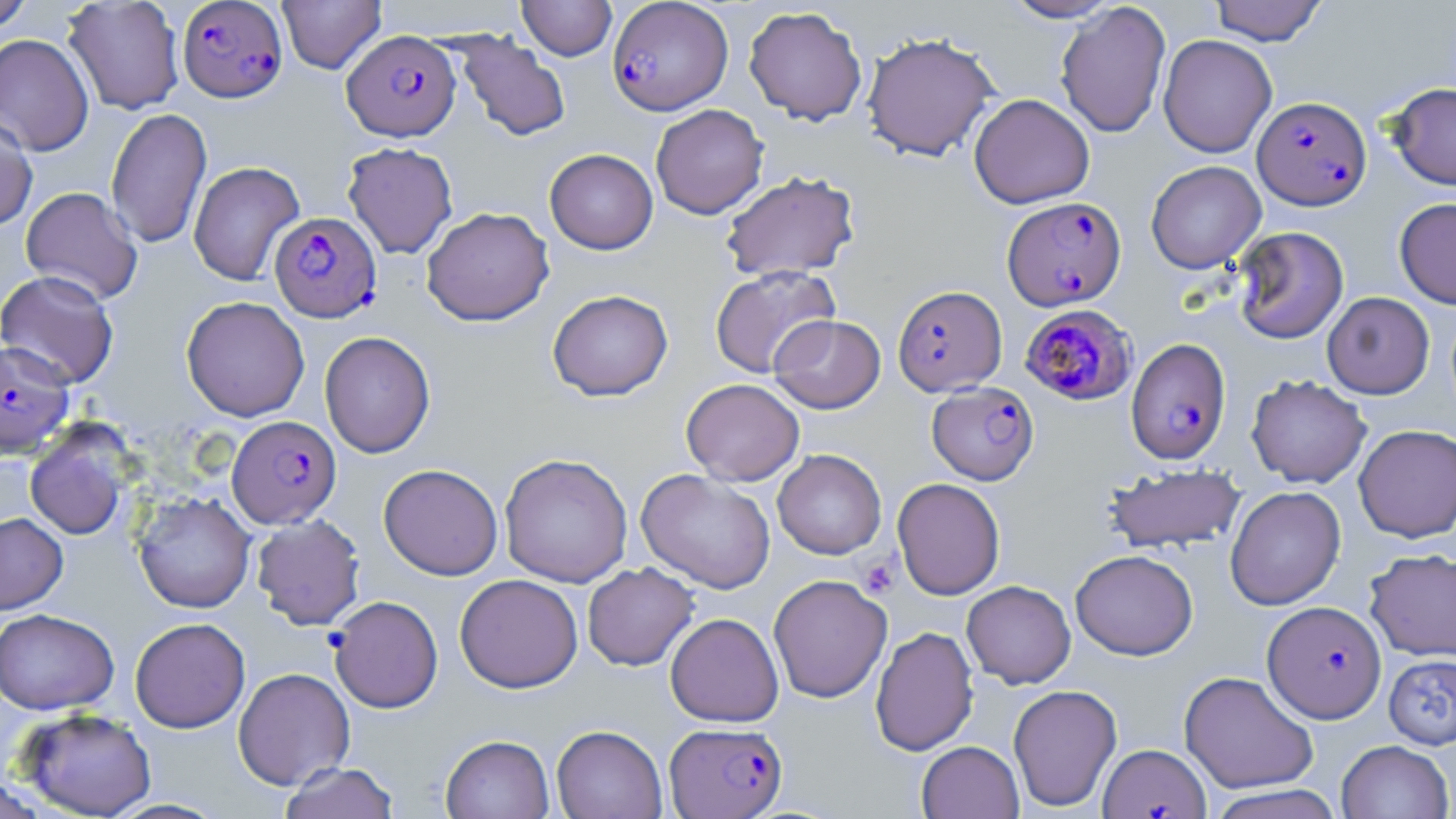 Approximate bounding boxes as (x1,y1)-(x2,y2) corner pairs in pixels. Uninfected red blood cell locations: (62,0)-(185,115), (277,0)-(386,74), (518,0)-(617,60), (1001,0)-(1122,22), (1209,0)-(1328,45), (0,1)-(36,34), (1056,2)-(1171,139), (744,6)-(868,125), (861,31)-(1000,162), (453,32)-(571,142), (0,33)-(94,156), (1158,34)-(1277,157), (1388,82)-(1456,190), (969,93)-(1095,209), (650,104)-(768,219), (106,108)-(212,248), (0,114)-(38,232), (342,141)-(458,259), (544,149)-(658,254), (1145,160)-(1266,274), (188,161)-(305,286), (720,170)-(861,282), (20,186)-(143,304), (1394,197)-(1456,309), (421,206)-(555,326), (1232,226)-(1349,344), (709,265)-(840,378), (0,270)-(120,388), (547,289)-(673,401), (1322,292)-(1435,398), (181,296)-(310,421), (769,314)-(886,413), (319,331)-(435,458), (1246,374)-(1372,488), (681,378)-(805,486), (1353,424)-(1456,542), (25,426)-(132,540), (772,449)-(886,559), (499,452)-(633,588), (379,463)-(503,580), (1103,464)-(1247,554), (636,468)-(776,593), (892,477)-(1005,600), (1224,485)-(1346,610), (133,492)-(256,613), (0,512)-(68,614), (251,514)-(365,630), (1364,547)-(1456,661), (1070,549)-(1198,660), (582,563)-(699,671), (454,574)-(583,693), (768,574)-(892,703), (961,580)-(1076,689), (0,608)-(119,714), (665,612)-(783,727), (130,617)-(250,733), (870,625)-(978,756), (1383,653)-(1456,750), (233,666)-(356,790), (1179,671)-(1319,794), (1008,684)-(1122,812), (16,708)-(157,819), (551,724)-(667,819), (441,734)-(554,819), (1335,739)-(1454,818), (917,740)-(1023,818), (278,761)-(401,819), (1205,784)-(1347,819). Platelet locations: (857,555)-(900,599). Plasmodium falciparum-infected red blood cell locations: (177,0)-(288,102), (607,0)-(733,115), (343,29)-(460,141), (1253,96)-(1371,210), (1002,196)-(1126,311), (270,212)-(381,323), (892,284)-(1007,396), (1017,304)-(1140,407), (1125,338)-(1231,465), (0,339)-(75,457), (927,382)-(1039,485), (227,415)-(341,528), (328,595)-(443,713), (1262,600)-(1387,723), (664,721)-(787,818), (1099,744)-(1210,818). Slide-level diagnosis: Plasmodium falciparum. Image is 1456×819 pixels. One field of a larger specimen. Thin blood smear. Optical microscopy. May-Grünwald-Giemsa stain. Captured at 1000x magnification.